Name the blood parasite species.
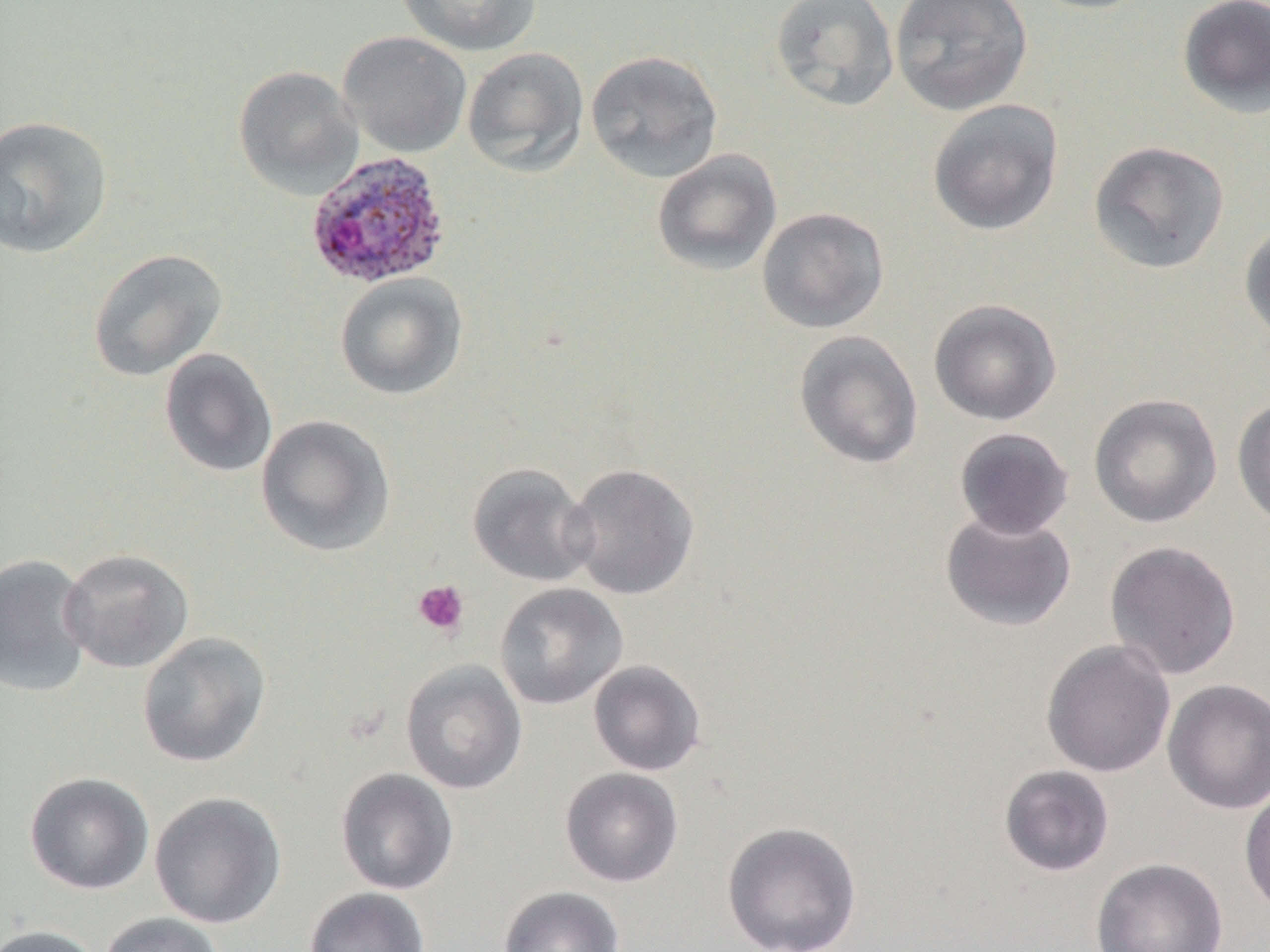
Plasmodium ovale.

Summary:
  - Coordinate format: approximate bounding boxes as named x1/y1/x2/y2 corners in pixels
  - Plasmodium ovale-infected red blood cell locations: (x1=304, y1=151, x2=451, y2=290)
  - Platelet locations: (x1=412, y1=580, x2=470, y2=638)
  - Uninfected red blood cell locations: (x1=395, y1=0, x2=543, y2=57), (x1=770, y1=0, x2=899, y2=112), (x1=890, y1=0, x2=1033, y2=116), (x1=1025, y1=0, x2=1155, y2=14), (x1=1177, y1=1, x2=1270, y2=119), (x1=338, y1=31, x2=471, y2=158), (x1=462, y1=47, x2=589, y2=177), (x1=585, y1=49, x2=724, y2=182), (x1=233, y1=65, x2=364, y2=199), (x1=927, y1=99, x2=1064, y2=237), (x1=0, y1=114, x2=115, y2=260), (x1=1088, y1=140, x2=1230, y2=274), (x1=651, y1=148, x2=783, y2=277), (x1=756, y1=206, x2=890, y2=334), (x1=1239, y1=220, x2=1270, y2=348), (x1=87, y1=248, x2=228, y2=382), (x1=334, y1=272, x2=467, y2=400), (x1=928, y1=299, x2=1062, y2=426), (x1=793, y1=330, x2=924, y2=470), (x1=158, y1=348, x2=278, y2=479), (x1=1088, y1=393, x2=1223, y2=529), (x1=1231, y1=397, x2=1270, y2=529), (x1=255, y1=414, x2=396, y2=556), (x1=954, y1=427, x2=1075, y2=540), (x1=563, y1=462, x2=700, y2=600), (x1=467, y1=463, x2=598, y2=587), (x1=940, y1=509, x2=1077, y2=632), (x1=1104, y1=540, x2=1242, y2=680), (x1=60, y1=548, x2=195, y2=673), (x1=0, y1=554, x2=93, y2=697), (x1=494, y1=582, x2=628, y2=710), (x1=137, y1=632, x2=271, y2=769), (x1=1041, y1=639, x2=1176, y2=778), (x1=400, y1=659, x2=528, y2=794), (x1=588, y1=660, x2=707, y2=776), (x1=1162, y1=678, x2=1270, y2=815), (x1=998, y1=764, x2=1115, y2=877), (x1=559, y1=767, x2=684, y2=887), (x1=335, y1=768, x2=459, y2=895), (x1=24, y1=772, x2=155, y2=895), (x1=1239, y1=785, x2=1270, y2=917), (x1=149, y1=791, x2=287, y2=929), (x1=721, y1=820, x2=863, y2=952), (x1=1090, y1=857, x2=1228, y2=952), (x1=497, y1=885, x2=626, y2=952), (x1=303, y1=887, x2=430, y2=952), (x1=97, y1=912, x2=227, y2=952), (x1=0, y1=924, x2=106, y2=952)
  - Image size: 1270×952 pixels
  - Modality: light microscopy
  - Field of view: one of a larger specimen
  - Magnification: 1000x
  - Preparation: thin blood film